Outline each uninfected red blood cell.
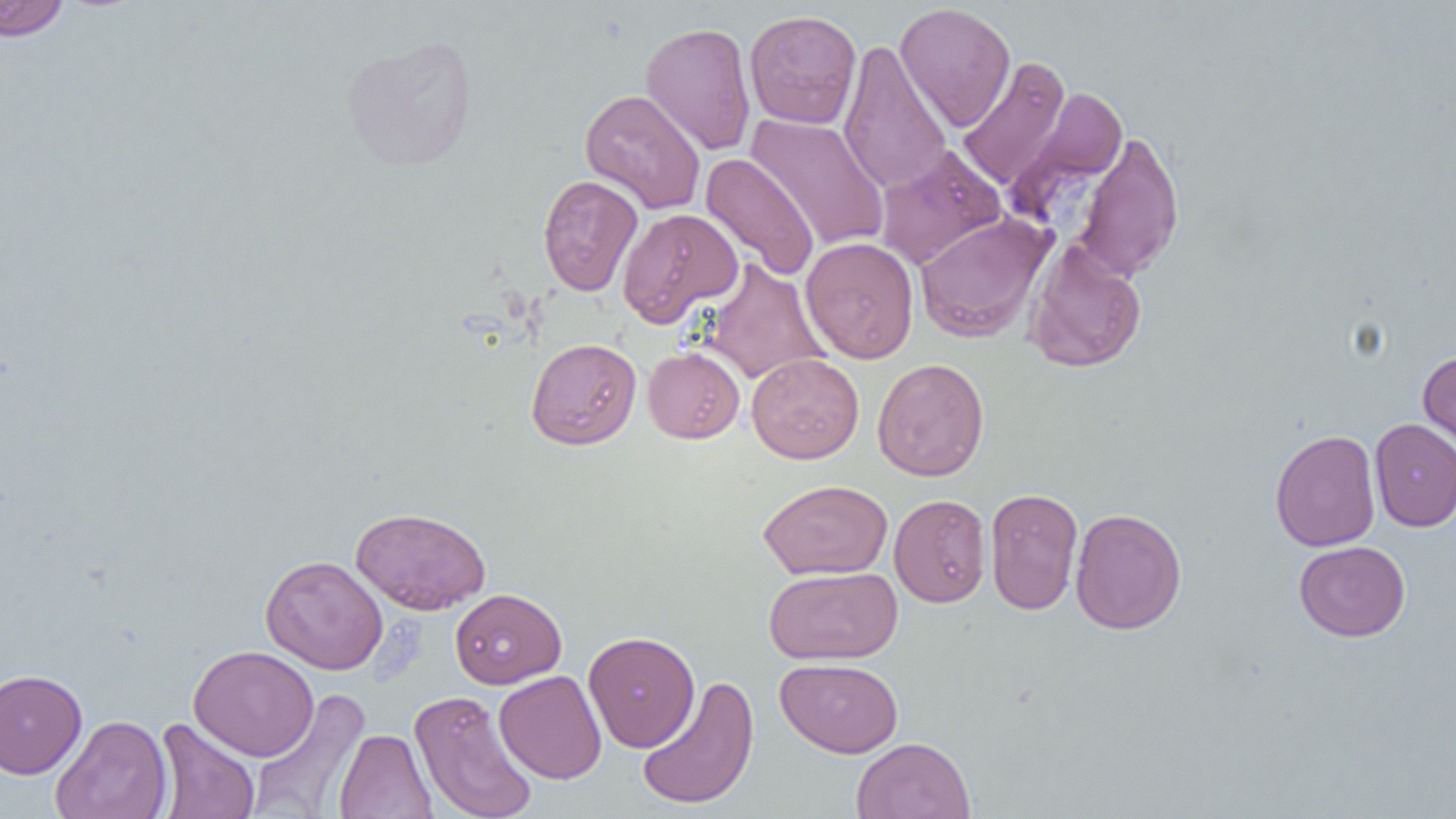
Approximate bounding boxes as named x1/y1/x2/y2 corners in pixels.
Uninfected red blood cells: (x1=0, y1=0, x2=72, y2=42), (x1=895, y1=2, x2=1016, y2=131), (x1=744, y1=9, x2=862, y2=129), (x1=640, y1=21, x2=756, y2=156), (x1=340, y1=34, x2=479, y2=171), (x1=838, y1=38, x2=952, y2=194), (x1=956, y1=56, x2=1071, y2=191), (x1=1007, y1=85, x2=1129, y2=217), (x1=579, y1=88, x2=706, y2=214), (x1=746, y1=113, x2=890, y2=251), (x1=1074, y1=130, x2=1185, y2=282), (x1=873, y1=144, x2=1006, y2=270), (x1=700, y1=153, x2=819, y2=281), (x1=538, y1=175, x2=643, y2=296), (x1=616, y1=207, x2=743, y2=327), (x1=913, y1=212, x2=1055, y2=343), (x1=800, y1=236, x2=919, y2=363), (x1=1025, y1=238, x2=1147, y2=373), (x1=701, y1=259, x2=828, y2=385), (x1=526, y1=337, x2=642, y2=450), (x1=643, y1=347, x2=745, y2=443), (x1=1418, y1=349, x2=1456, y2=459), (x1=746, y1=353, x2=864, y2=463), (x1=872, y1=358, x2=989, y2=482), (x1=1369, y1=418, x2=1456, y2=532), (x1=1269, y1=429, x2=1381, y2=552), (x1=758, y1=478, x2=893, y2=580), (x1=984, y1=487, x2=1083, y2=615), (x1=889, y1=494, x2=991, y2=608), (x1=350, y1=507, x2=491, y2=614), (x1=1070, y1=507, x2=1187, y2=635), (x1=1294, y1=540, x2=1410, y2=642), (x1=260, y1=555, x2=388, y2=674), (x1=764, y1=566, x2=903, y2=665), (x1=450, y1=588, x2=566, y2=689), (x1=583, y1=630, x2=700, y2=752), (x1=188, y1=645, x2=319, y2=760), (x1=775, y1=658, x2=903, y2=757), (x1=0, y1=669, x2=88, y2=779), (x1=494, y1=670, x2=607, y2=784), (x1=636, y1=675, x2=760, y2=810), (x1=247, y1=689, x2=370, y2=818), (x1=410, y1=689, x2=537, y2=819), (x1=51, y1=714, x2=172, y2=819), (x1=153, y1=718, x2=260, y2=819), (x1=333, y1=728, x2=437, y2=819), (x1=851, y1=736, x2=975, y2=819).

Slide-level diagnosis: no evidence of blood parasites. Optical microscopy. Single field of view. Captured at 1000x magnification. Thin blood film. Image is 1456×819 pixels.